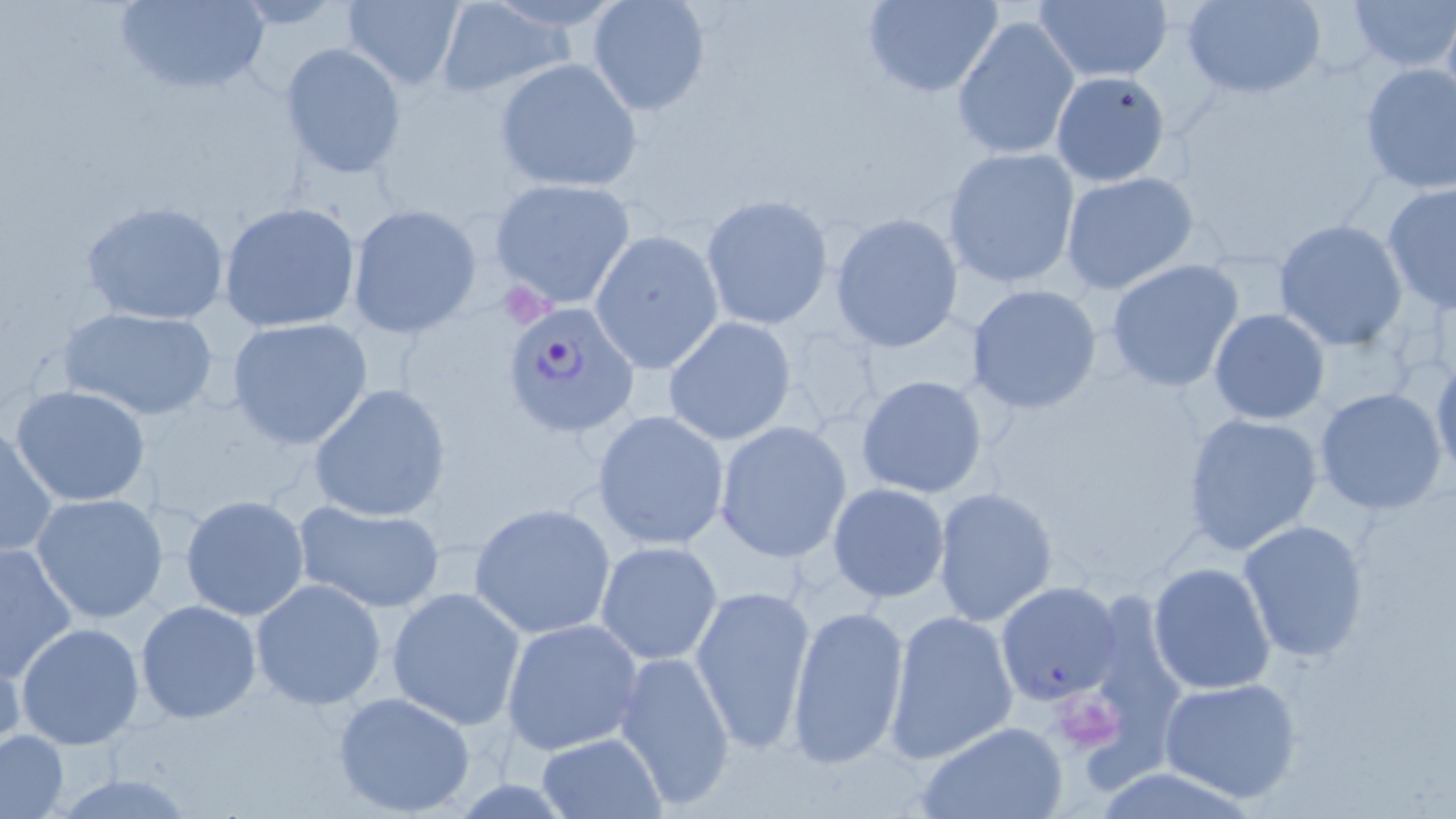 Approximate bounding boxes as named x1/y1/x2/y2 corners in pixels. Uninfected red blood cell locations: (x1=110, y1=0, x2=271, y2=98), (x1=586, y1=0, x2=711, y2=117), (x1=860, y1=0, x2=1005, y2=97), (x1=1182, y1=0, x2=1327, y2=99), (x1=1347, y1=0, x2=1456, y2=71), (x1=339, y1=1, x2=465, y2=89), (x1=433, y1=1, x2=574, y2=98), (x1=1033, y1=1, x2=1172, y2=84), (x1=952, y1=16, x2=1079, y2=162), (x1=278, y1=42, x2=407, y2=179), (x1=494, y1=57, x2=643, y2=194), (x1=1358, y1=62, x2=1456, y2=197), (x1=1050, y1=70, x2=1172, y2=188), (x1=942, y1=146, x2=1081, y2=289), (x1=1060, y1=171, x2=1203, y2=298), (x1=490, y1=179, x2=636, y2=310), (x1=1381, y1=183, x2=1456, y2=313), (x1=700, y1=195, x2=834, y2=329), (x1=81, y1=201, x2=231, y2=325), (x1=218, y1=202, x2=362, y2=334), (x1=347, y1=203, x2=484, y2=338), (x1=830, y1=213, x2=963, y2=353), (x1=1272, y1=220, x2=1408, y2=351), (x1=589, y1=231, x2=723, y2=373), (x1=1105, y1=259, x2=1245, y2=392), (x1=967, y1=284, x2=1103, y2=415), (x1=59, y1=306, x2=219, y2=422), (x1=1209, y1=308, x2=1329, y2=425), (x1=226, y1=317, x2=373, y2=450), (x1=662, y1=317, x2=799, y2=446), (x1=1430, y1=354, x2=1455, y2=487), (x1=856, y1=375, x2=989, y2=499), (x1=9, y1=384, x2=153, y2=508), (x1=309, y1=384, x2=452, y2=522), (x1=1314, y1=387, x2=1450, y2=516), (x1=591, y1=409, x2=730, y2=551), (x1=1182, y1=411, x2=1324, y2=556), (x1=715, y1=421, x2=853, y2=561), (x1=0, y1=422, x2=58, y2=561), (x1=827, y1=483, x2=951, y2=602), (x1=931, y1=487, x2=1058, y2=625), (x1=29, y1=492, x2=170, y2=625), (x1=179, y1=494, x2=311, y2=620), (x1=293, y1=499, x2=447, y2=613), (x1=468, y1=502, x2=616, y2=639), (x1=1237, y1=519, x2=1369, y2=661), (x1=425, y1=530, x2=609, y2=696), (x1=595, y1=540, x2=724, y2=665), (x1=0, y1=541, x2=78, y2=681), (x1=1147, y1=560, x2=1277, y2=696), (x1=250, y1=578, x2=386, y2=707), (x1=995, y1=579, x2=1124, y2=705), (x1=690, y1=581, x2=817, y2=753), (x1=386, y1=586, x2=528, y2=729), (x1=135, y1=600, x2=262, y2=723), (x1=785, y1=602, x2=911, y2=770), (x1=883, y1=608, x2=1019, y2=765), (x1=500, y1=617, x2=646, y2=756), (x1=15, y1=622, x2=145, y2=749), (x1=0, y1=639, x2=26, y2=755), (x1=615, y1=647, x2=736, y2=813), (x1=1156, y1=677, x2=1303, y2=804), (x1=333, y1=691, x2=477, y2=818), (x1=913, y1=721, x2=1070, y2=819), (x1=1, y1=730, x2=68, y2=816), (x1=538, y1=733, x2=665, y2=817), (x1=1086, y1=766, x2=1264, y2=818). Plasmodium falciparum-infected red blood cell locations: (x1=504, y1=300, x2=639, y2=435). Platelet locations: (x1=1056, y1=700, x2=1122, y2=753). Slide-level diagnosis: Plasmodium falciparum. Image is 1456×819 pixels. Optical microscopy. May-Grünwald-Giemsa stain. 1000x magnification. Single field of view. Thin blood film.